Locate every Plasmodium parasite and every leukocyte.
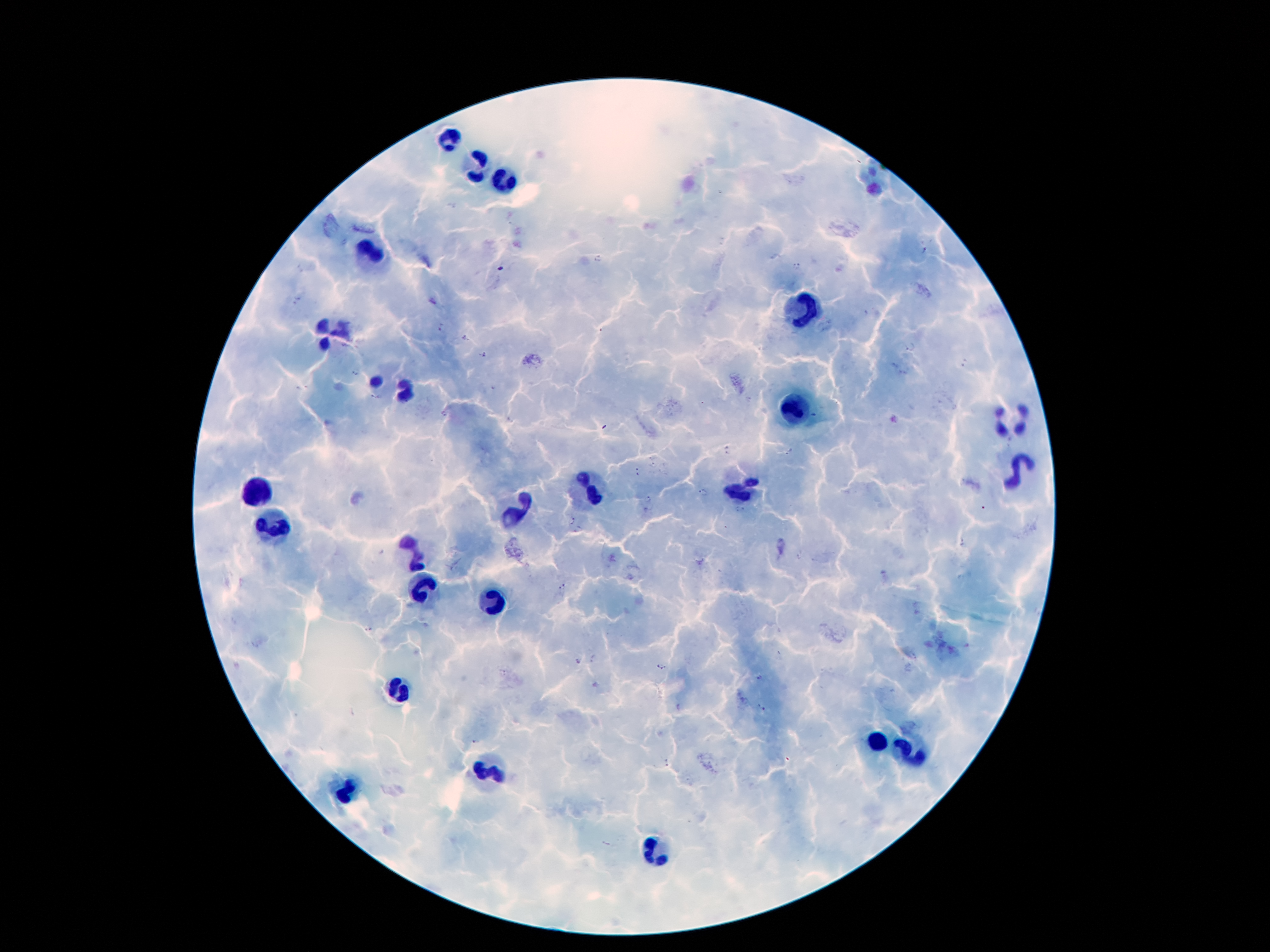

Approximate object centers, in pixels from the top-left corner.
Plasmodium parasites: (x=924, y=251), (x=600, y=259), (x=796, y=266), (x=296, y=302), (x=443, y=328), (x=466, y=337), (x=910, y=347), (x=482, y=356), (x=356, y=372), (x=377, y=396), (x=442, y=414), (x=511, y=420), (x=727, y=450), (x=790, y=451), (x=653, y=465), (x=637, y=471), (x=704, y=491), (x=648, y=499), (x=741, y=510), (x=573, y=520), (x=579, y=530), (x=963, y=544), (x=798, y=557), (x=564, y=587), (x=367, y=628), (x=594, y=658), (x=578, y=661), (x=661, y=666), (x=760, y=676), (x=761, y=707), (x=477, y=741), (x=667, y=762).
Leukocytes: (x=449, y=140), (x=477, y=167), (x=504, y=182), (x=371, y=253), (x=804, y=314), (x=331, y=333), (x=376, y=381), (x=405, y=391), (x=796, y=408), (x=1013, y=419), (x=1018, y=467), (x=588, y=488), (x=743, y=491), (x=259, y=492), (x=516, y=512), (x=275, y=528), (x=414, y=555), (x=423, y=582), (x=489, y=605), (x=401, y=685), (x=875, y=741), (x=907, y=755), (x=489, y=767), (x=350, y=791), (x=650, y=850).

Summary:
  - Field of view: single
  - Magnification: 100x
  - Patient malaria status: positive for Plasmodium falciparum
  - Stain: Giemsa
  - Image size: 1270×952 pixels
  - Preparation: thick blood smear
  - Capture: smartphone camera through the microscope eyepiece